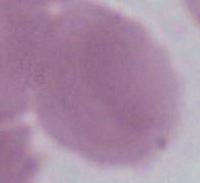
magnification = 1000x
modality = micrograph
identification = erythrocyte